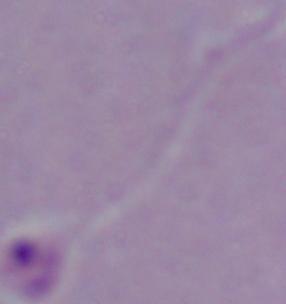

identification = Leishmania
modality = photomicrograph
magnification = 1000x